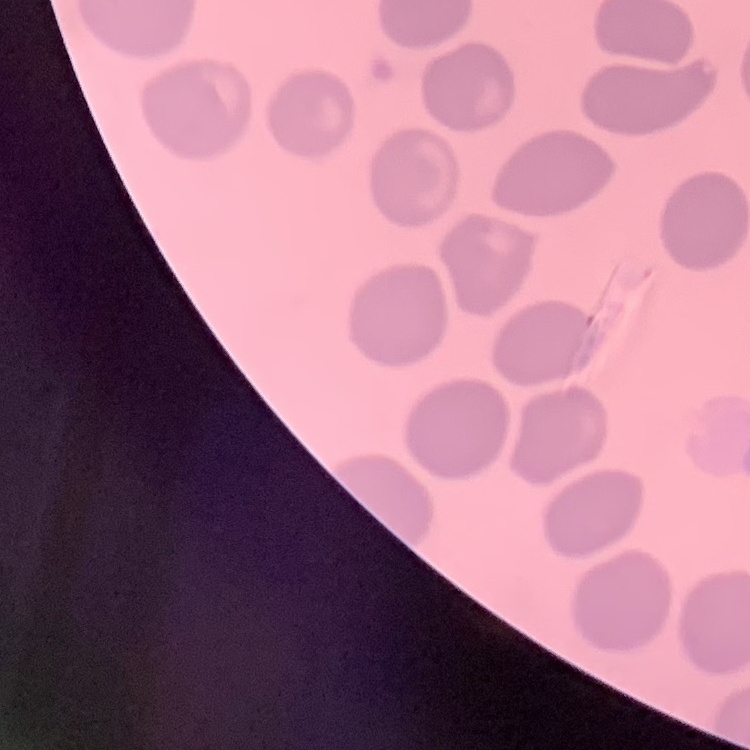
red blood cell morphology = no rouleaux formation
preparation = thin blood smear
stain = Field's or Giemsa
image type = one tile cut from a larger photomicrograph